Give the extent of all Plasmodium ovale-infected red blood cells.
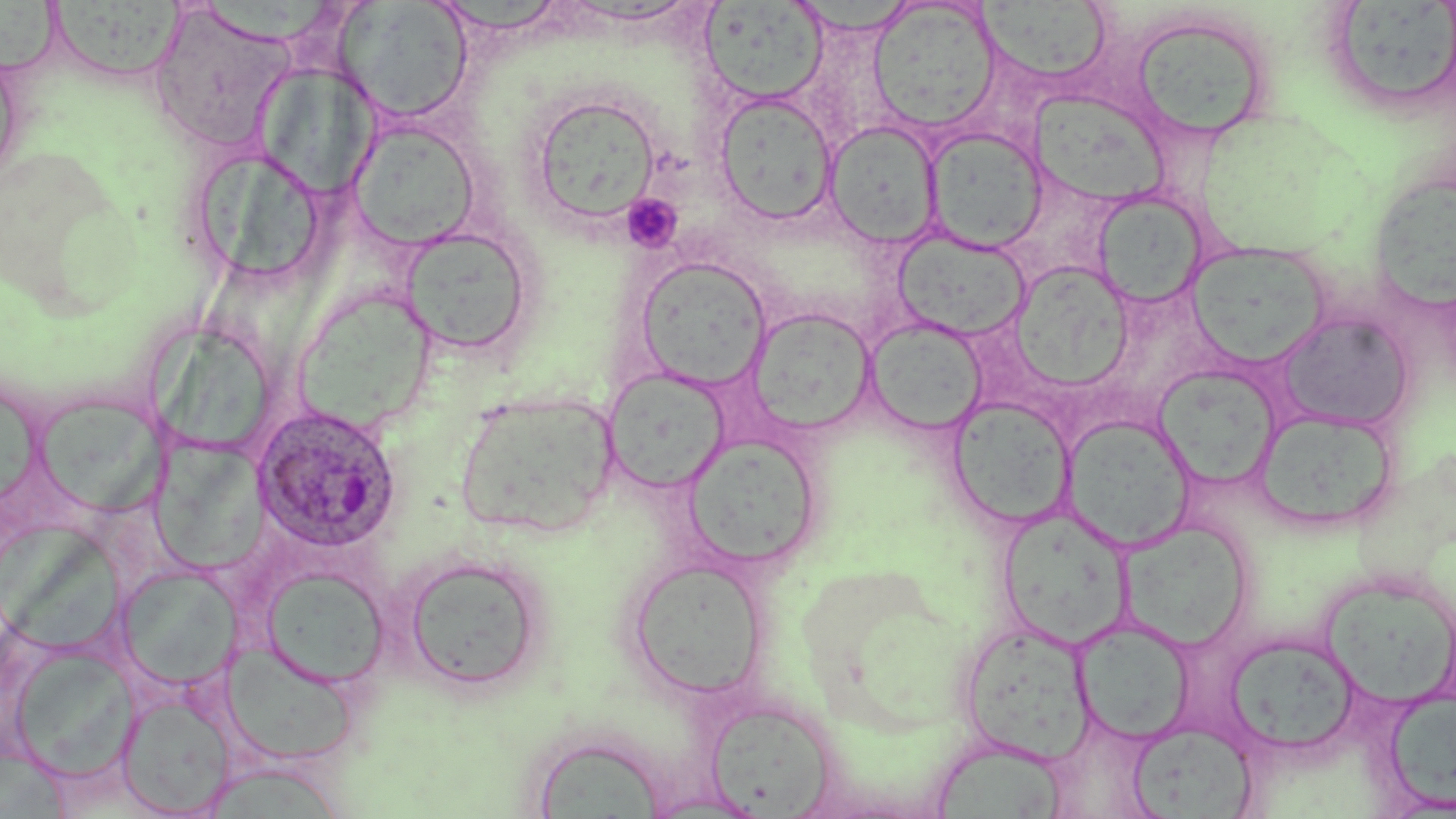
Approximate bounding boxes as named x1/y1/x2/y2 corners in pixels.
Plasmodium ovale-infected red blood cells: (x1=252, y1=404, x2=403, y2=552).

Platelet locations: (x1=621, y1=193, x2=683, y2=253). Uninfected red blood cell locations: (x1=1334, y1=0, x2=1455, y2=104), (x1=336, y1=1, x2=473, y2=123), (x1=787, y1=1, x2=924, y2=37), (x1=868, y1=1, x2=1002, y2=134), (x1=47, y1=2, x2=190, y2=76), (x1=701, y1=2, x2=828, y2=105), (x1=0, y1=3, x2=71, y2=80), (x1=977, y1=4, x2=1115, y2=83), (x1=144, y1=5, x2=293, y2=154), (x1=1130, y1=13, x2=1272, y2=142), (x1=0, y1=46, x2=24, y2=188), (x1=252, y1=62, x2=382, y2=198), (x1=526, y1=91, x2=664, y2=228), (x1=714, y1=92, x2=839, y2=225), (x1=1031, y1=93, x2=1178, y2=210), (x1=347, y1=119, x2=481, y2=252), (x1=825, y1=120, x2=943, y2=248), (x1=925, y1=127, x2=1047, y2=252), (x1=204, y1=153, x2=323, y2=278), (x1=1367, y1=171, x2=1456, y2=314), (x1=1092, y1=190, x2=1207, y2=310), (x1=399, y1=225, x2=536, y2=358), (x1=892, y1=229, x2=1030, y2=341), (x1=1188, y1=241, x2=1331, y2=367), (x1=634, y1=255, x2=770, y2=390), (x1=1009, y1=261, x2=1135, y2=393), (x1=298, y1=286, x2=441, y2=423), (x1=746, y1=305, x2=877, y2=437), (x1=1276, y1=312, x2=1415, y2=431), (x1=865, y1=318, x2=988, y2=436), (x1=147, y1=324, x2=277, y2=444), (x1=1154, y1=365, x2=1282, y2=489), (x1=603, y1=368, x2=730, y2=493), (x1=455, y1=390, x2=620, y2=539), (x1=30, y1=392, x2=164, y2=518), (x1=947, y1=395, x2=1076, y2=529), (x1=1254, y1=406, x2=1399, y2=533), (x1=1062, y1=414, x2=1194, y2=552), (x1=684, y1=433, x2=823, y2=568), (x1=151, y1=439, x2=269, y2=572), (x1=997, y1=507, x2=1135, y2=650), (x1=1120, y1=519, x2=1254, y2=650), (x1=401, y1=553, x2=549, y2=692), (x1=625, y1=558, x2=770, y2=700), (x1=116, y1=564, x2=242, y2=693), (x1=260, y1=566, x2=390, y2=689), (x1=1318, y1=582, x2=1452, y2=711), (x1=958, y1=619, x2=1096, y2=764), (x1=1074, y1=619, x2=1194, y2=744), (x1=1224, y1=633, x2=1362, y2=757), (x1=8, y1=642, x2=138, y2=781), (x1=223, y1=644, x2=361, y2=765), (x1=1381, y1=688, x2=1456, y2=811), (x1=118, y1=691, x2=235, y2=816), (x1=704, y1=698, x2=839, y2=815), (x1=1127, y1=721, x2=1257, y2=817), (x1=930, y1=743, x2=1070, y2=817), (x1=196, y1=761, x2=349, y2=817), (x1=641, y1=791, x2=769, y2=818). Slide-level diagnosis: Plasmodium ovale. May-Grünwald-Giemsa-stained preparation. Thin blood smear. Image is 1456×819 pixels. Captured at 1000x magnification. One field of a larger specimen. Light microscopy.